Assess the morphology of the erythrocytes.
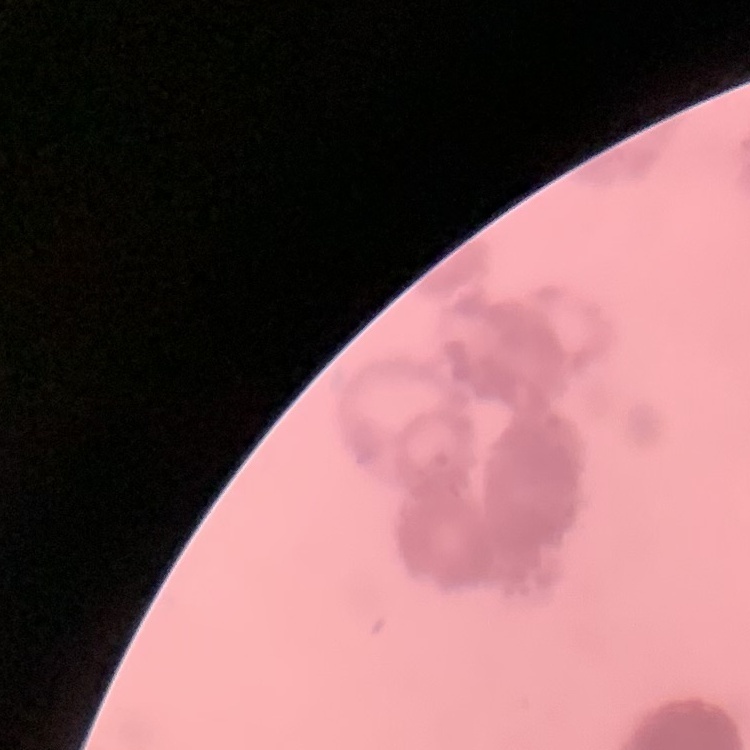
Rouleaux formation.

Thin blood film. Square crop of a larger photomicrograph. Stained with either Field's or Giemsa.